Name the cell type shown.
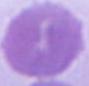
This is an erythrocyte.

Captured at 1000x magnification. Micrograph.